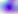

Summary:
  - Identification: Toxoplasma gondii
  - Modality: micrograph
  - Magnification: 400x